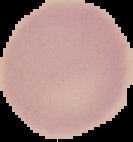 Result: no malaria parasites detected. Image is 133×142 pixels. From a thin blood film. Segmented cell region on a black background.